Assess the morphology of the red blood cells.
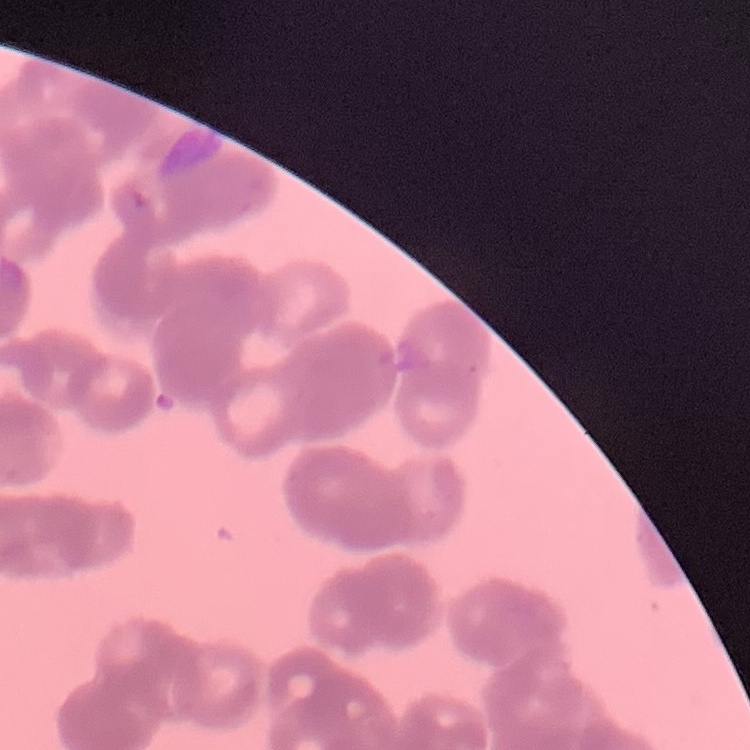

They show rouleaux formation.

Field's or Giemsa stain. Thin peripheral smear. One tile cut from a larger photomicrograph.